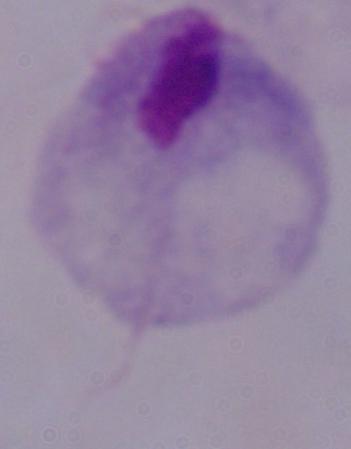
Micrograph. 1000x magnification. A trichomonad is shown.